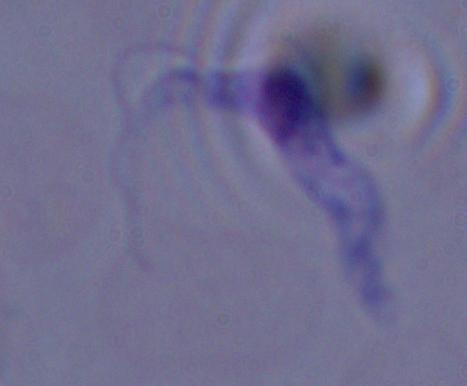
magnification: 1000x
identification: trypanosome
modality: micrograph